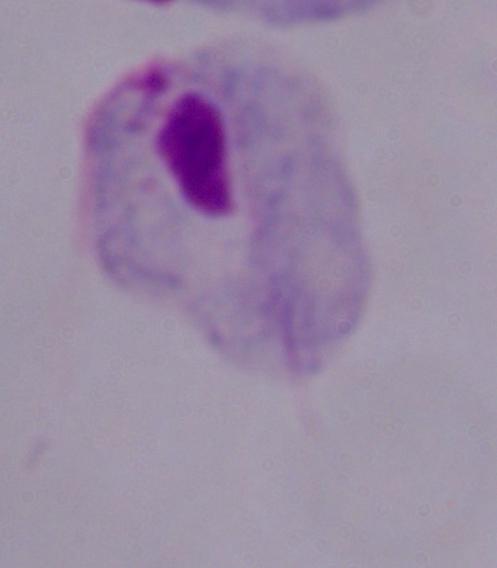
identification = trichomonad
magnification = 1000x
modality = photomicrograph